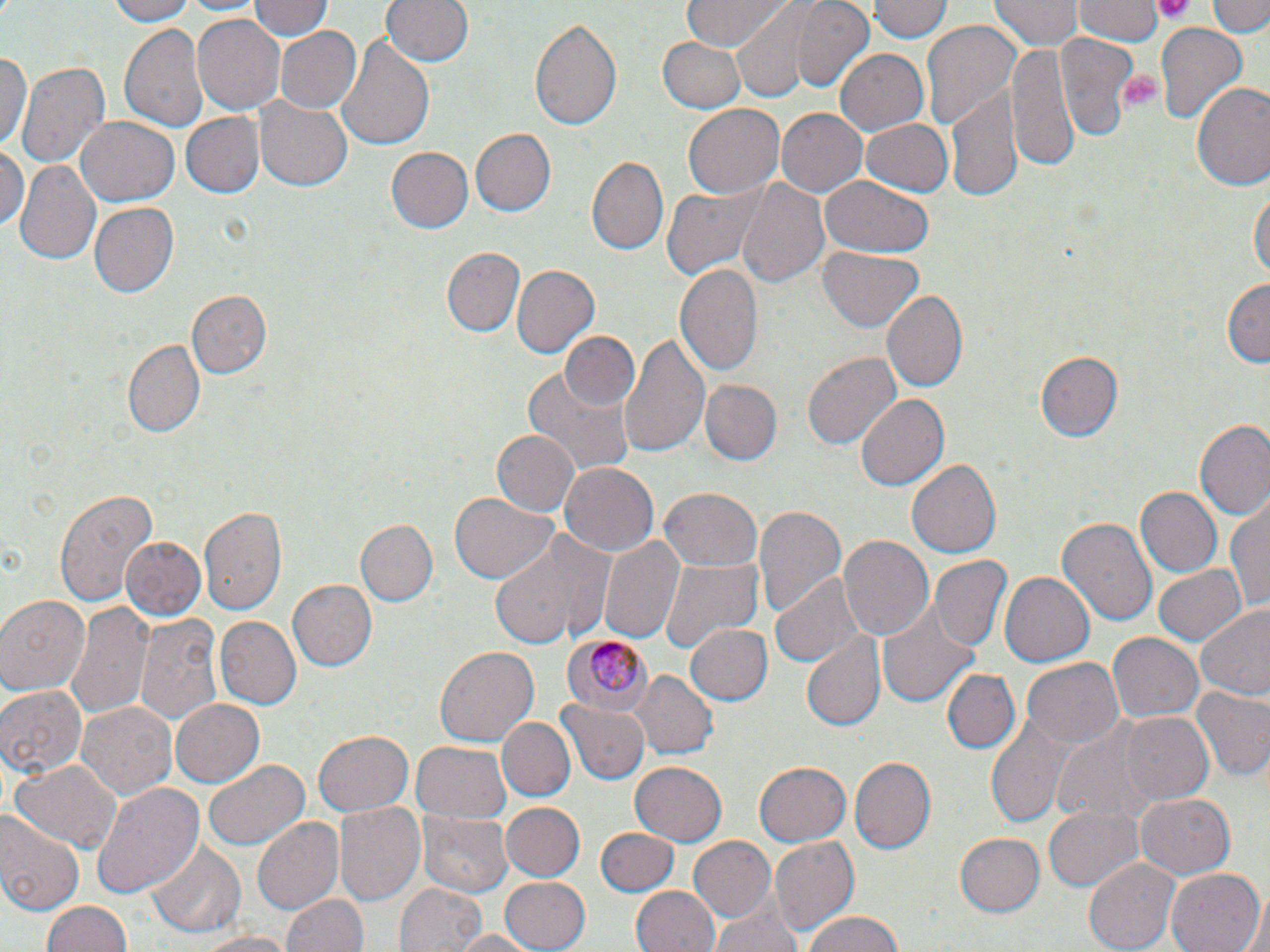

Summary:
  - Coordinate format: approximate bounding boxes as (x1,y1)-(x2,y2) corner pairs in pixels
  - Uninfected red blood cell locations: (104,0)-(203,25), (248,0)-(333,42), (381,0)-(472,66), (679,0)-(795,50), (870,0)-(952,45), (992,0)-(1079,50), (1209,0)-(1268,35), (792,1)-(877,90), (1073,1)-(1164,45), (727,3)-(838,99), (192,14)-(284,115), (529,14)-(624,134), (119,19)-(210,134), (921,20)-(1023,134), (1153,24)-(1248,128), (275,26)-(364,114), (1056,31)-(1137,141), (333,34)-(434,152), (659,35)-(748,113), (1006,39)-(1079,176), (835,49)-(928,134), (0,51)-(31,156), (17,62)-(109,170), (1192,81)-(1270,194), (945,85)-(1023,200), (257,98)-(352,190), (683,104)-(785,199), (775,108)-(866,198), (180,112)-(264,198), (75,116)-(179,207), (860,117)-(952,196), (469,128)-(556,217), (0,145)-(27,233), (387,146)-(473,233), (586,154)-(668,253), (13,159)-(101,268), (821,176)-(932,256), (736,177)-(830,291), (661,184)-(765,280), (1250,185)-(1268,288), (87,202)-(178,298), (821,244)-(924,330), (444,247)-(524,336), (675,260)-(763,378), (510,264)-(596,358), (1222,277)-(1269,366), (185,290)-(270,378), (882,290)-(968,392), (561,330)-(637,409), (621,332)-(710,458), (123,340)-(205,439), (1034,349)-(1124,440), (803,350)-(901,449), (522,363)-(635,475), (699,379)-(781,465), (853,394)-(947,491), (1195,421)-(1270,524), (489,429)-(578,517), (906,459)-(1001,556), (559,462)-(658,555), (54,485)-(156,609), (660,487)-(762,571), (1136,487)-(1221,578), (450,492)-(555,584), (1225,501)-(1270,608), (751,505)-(845,621), (200,506)-(288,615), (1057,515)-(1158,626), (356,519)-(437,608), (487,531)-(614,649), (598,533)-(683,643), (839,534)-(934,639), (121,536)-(207,620), (932,555)-(1011,650), (657,556)-(763,654), (1153,562)-(1245,646), (771,570)-(862,666), (1001,573)-(1094,665), (286,578)-(376,673), (0,596)-(88,695), (877,597)-(982,706), (67,601)-(152,718), (1197,602)-(1270,703), (138,612)-(219,724), (214,616)-(301,710), (687,625)-(772,704), (803,633)-(885,730), (1107,633)-(1202,723), (434,645)-(538,748), (1023,658)-(1124,748), (942,667)-(1019,753), (634,670)-(718,758), (0,684)-(87,779), (1190,687)-(1269,782), (78,699)-(176,799), (169,699)-(265,788), (558,699)-(650,784), (986,709)-(1078,826), (1118,712)-(1214,805), (498,714)-(575,801), (1053,719)-(1159,828), (311,731)-(413,817), (412,742)-(510,822), (850,756)-(936,854), (204,757)-(309,850), (13,759)-(121,854), (753,762)-(850,846), (628,763)-(725,844), (89,783)-(204,898), (1134,793)-(1234,878), (331,802)-(425,908), (502,802)-(583,880), (1044,804)-(1144,892), (420,810)-(510,899), (0,813)-(83,918), (251,818)-(343,917), (597,827)-(676,897), (955,834)-(1044,915), (689,836)-(778,923), (770,837)-(859,935), (147,840)-(245,937), (1083,856)-(1180,951), (1167,869)-(1263,952), (498,876)-(591,952), (394,882)-(486,952), (630,884)-(719,952), (281,891)-(367,952), (710,896)-(803,952), (41,898)-(130,952), (1233,899)-(1270,952), (800,911)-(908,952), (448,929)-(539,952), (193,930)-(296,952)
  - Platelet locations: (1149,0)-(1196,21), (1121,71)-(1165,110)
  - Plasmodium malariae-infected red blood cell locations: (562,632)-(654,713)
  - Slide-level diagnosis: Plasmodium malariae
  - Modality: light microscopy
  - Magnification: 1000x
  - Stain: May-Grünwald-Giemsa
  - Preparation: thin blood film
  - Image size: 1270×952 pixels
  - Field of view: one of a larger specimen